Identify the parasite.
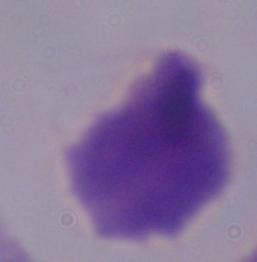
This is a trichomonad.

magnification = 1000x
modality = photomicrograph